Report the malaria status of this cell.
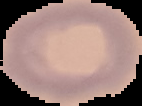
It is uninfected.

{
  "image_size": "142×106 pixels",
  "image_type": "segmented cell region on a black background",
  "preparation": "thin blood film"
}